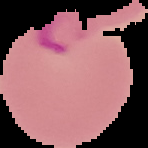

Summary:
  - Image type: segmented cell region on a black background
  - Image size: 148×148 pixels
  - Preparation: thin blood smear
  - Result: no malaria parasites seen